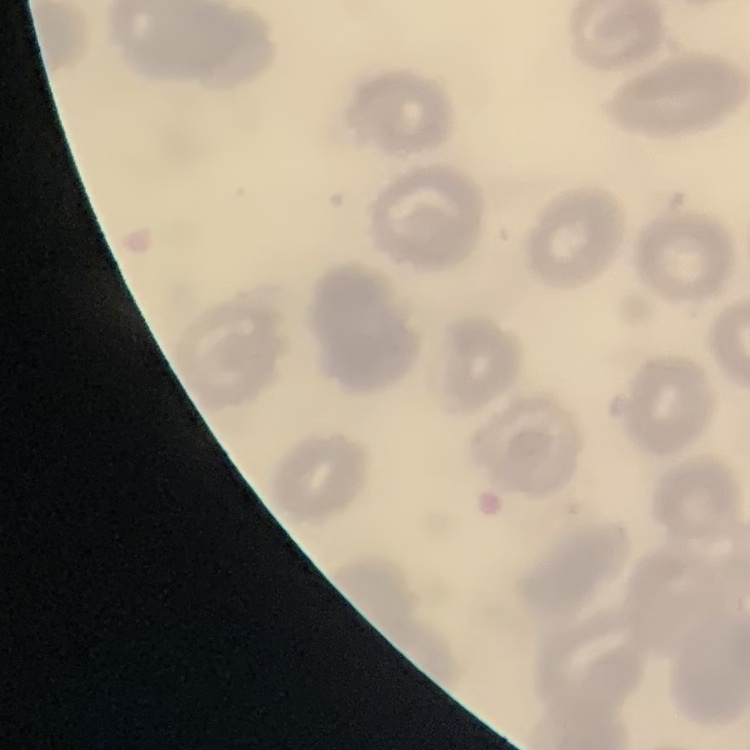

Summary:
  - Erythrocyte morphology: no rouleaux formation
  - Preparation: thin blood smear
  - Image type: one tile cut from a larger photomicrograph
  - Stain: Field's or Giemsa